Report the malaria status of this cell.
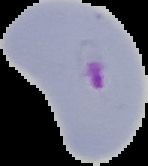

It is parasitized.

Segmented cell region on a black background. From a thin blood smear. Image is 148×166 pixels.